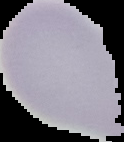

Image is 124×142 pixels. Result: no Plasmodium parasites seen. From a thin blood smear. The area outside the segmented cell region is set to black.